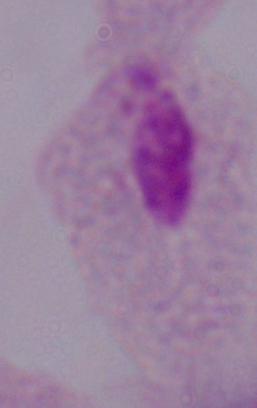

Summary:
  - Magnification: 1000x
  - Identification: trichomonad
  - Modality: photomicrograph